Report the malaria status of this cell.
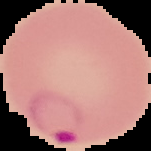
It is parasitized.

image size = 151×151 pixels
image type = segmented cell region with the area outside set to black
preparation = thin blood smear